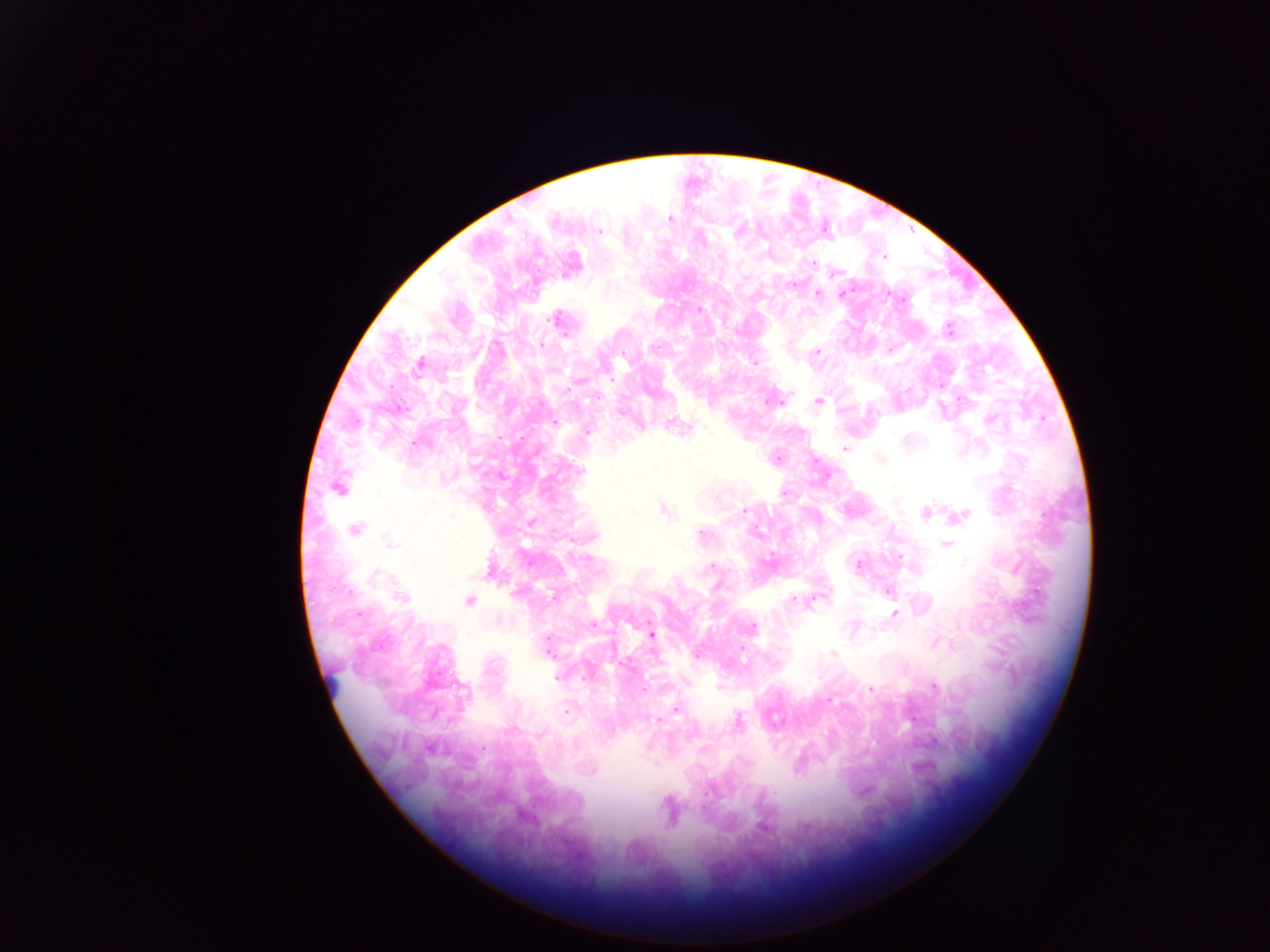 Approximate centers as {x, y} in pixels. Leukocyte locations: {334, 680}. Malaria parasite locations: {669, 219}, {599, 232}, {883, 257}, {571, 264}, {834, 273}, {792, 285}, {818, 293}, {841, 295}, {558, 319}, {948, 329}, {541, 344}, {816, 352}, {754, 361}, {419, 366}, {775, 401}, {819, 401}, {398, 409}, {622, 410}, {679, 426}, {587, 432}, {415, 443}, {845, 448}, {776, 457}, {500, 476}, {338, 488}, {662, 509}, {743, 511}, {926, 512}, {960, 515}, {530, 522}, {355, 529}, {700, 536}, {390, 543}, {947, 544}, {711, 565}, {858, 565}, {491, 570}, {887, 590}, {401, 596}, {813, 598}, {468, 601}, {893, 613}, {593, 624}, {751, 628}, {651, 635}, {549, 646}, {698, 653}, {832, 653}, {557, 677}, {933, 686}, {871, 689}, {676, 708}, {566, 710}, {654, 718}, {668, 809}. Image is 1270×952 pixels. Collected in Ghana. Photographed through a microscope with a mobile-phone camera. Single field of view. Thick blood film.